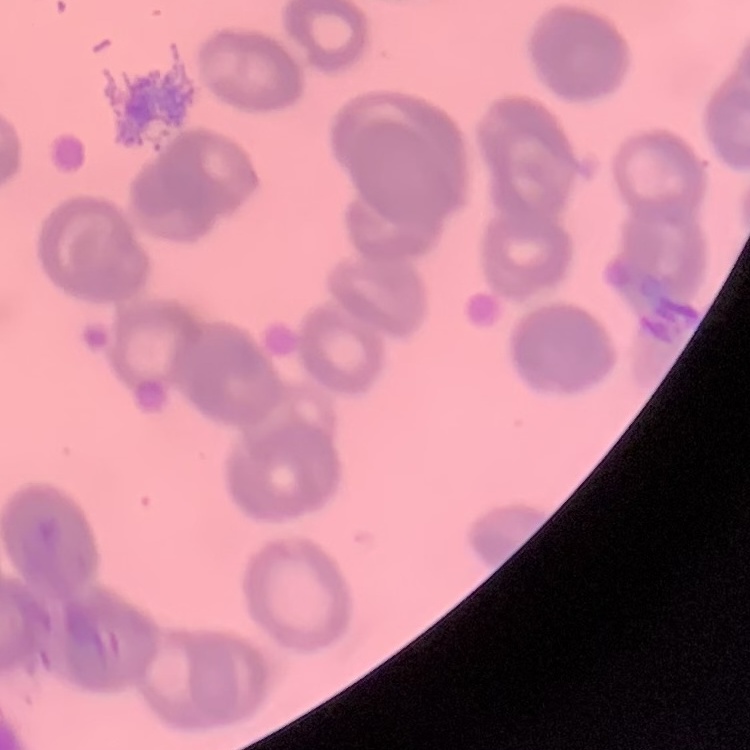 The red blood cells exhibit rouleaux formation. Field's or Giemsa stain. Thin blood film. Square crop of a larger photomicrograph.